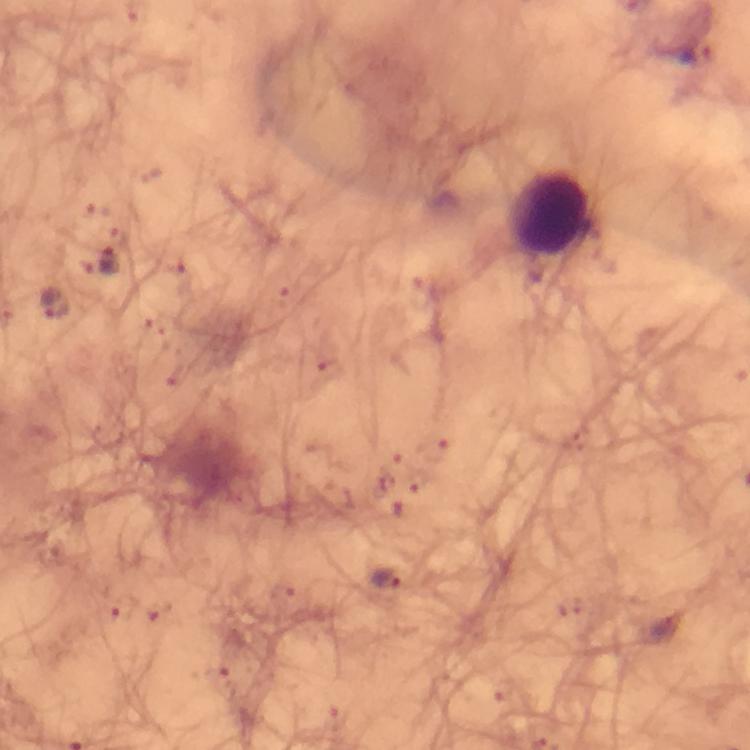
Approximate centers as (x, y) in pixels. Leukocyte locations: (550, 214). Malaria parasite locations: (696, 51), (106, 264), (55, 304), (389, 579), (665, 624). Photographed through the microscope with a smartphone camera. From a malaria diagnostic workup. Image is 750×750 pixels. 100x magnification. Immersion oil was used. Giemsa stain. Thick smear. A crop from one field of view.